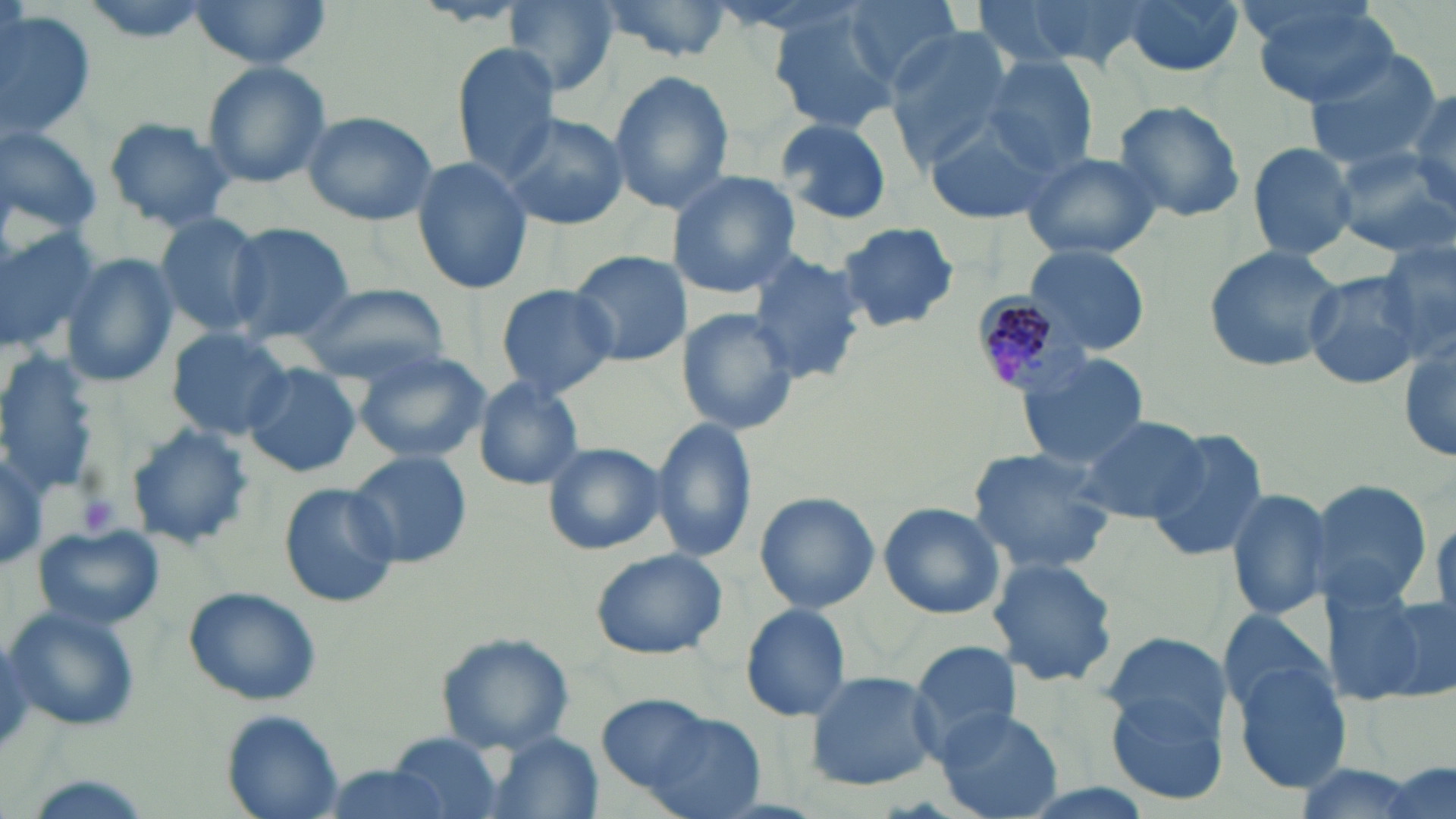
Approximate bounding boxes as (x1,y1)-(x2,y2) corner pairs in pixels. Platelet locations: (75,491)-(121,535). Plasmodium malariae-infected red blood cell locations: (969,287)-(1085,397). Uninfected red blood cell locations: (186,0)-(333,71), (501,0)-(618,95), (599,0)-(734,62), (835,0)-(964,93), (987,0)-(1155,72), (1117,0)-(1246,79), (1245,1)-(1400,107), (0,8)-(98,141), (767,9)-(900,132), (884,28)-(1015,166), (452,44)-(559,176), (1302,46)-(1447,170), (978,55)-(1099,176), (200,61)-(333,189), (607,69)-(734,216), (1405,88)-(1456,209), (1111,99)-(1246,222), (300,110)-(439,226), (499,111)-(629,231), (923,113)-(1057,222), (772,116)-(894,222), (105,117)-(236,231), (0,125)-(103,237), (1243,141)-(1358,260), (1330,147)-(1456,255), (1017,148)-(1165,262), (410,155)-(535,298), (666,171)-(801,297), (153,214)-(268,334), (222,221)-(356,344), (836,222)-(960,334), (0,225)-(100,350), (1376,237)-(1455,364), (1204,244)-(1341,373), (1022,245)-(1153,356), (568,249)-(690,365), (751,251)-(872,385), (62,255)-(178,388), (1303,269)-(1428,391), (294,281)-(449,384), (496,283)-(619,398), (680,308)-(800,438), (165,326)-(295,438), (1398,342)-(1455,464), (354,352)-(488,462), (0,353)-(97,489), (1019,353)-(1149,468), (242,363)-(362,478), (474,377)-(586,490), (1079,413)-(1208,523), (654,420)-(759,562), (126,424)-(253,551), (1146,428)-(1270,562), (543,442)-(667,554), (967,447)-(1119,574), (350,452)-(474,567), (1309,478)-(1431,609), (277,482)-(401,608), (1225,486)-(1336,622), (754,492)-(880,613), (878,501)-(1007,620), (33,524)-(165,631), (589,546)-(729,661), (987,554)-(1122,690), (1324,583)-(1452,707), (183,586)-(322,705), (740,604)-(851,722), (6,605)-(142,732), (1215,607)-(1335,716), (436,632)-(572,753), (1102,640)-(1236,810), (909,641)-(1021,762), (1228,659)-(1350,793), (804,670)-(940,790), (596,693)-(755,816), (934,710)-(1064,819), (222,711)-(341,817), (386,732)-(505,819), (478,732)-(605,819), (320,764)-(455,818). Slide-level diagnosis: Plasmodium malariae. 1000x magnification. Image is 1456×819 pixels. May-Grünwald-Giemsa-stained preparation. Single field of view. Optical microscopy. Thin blood film.